Give the preparation type.
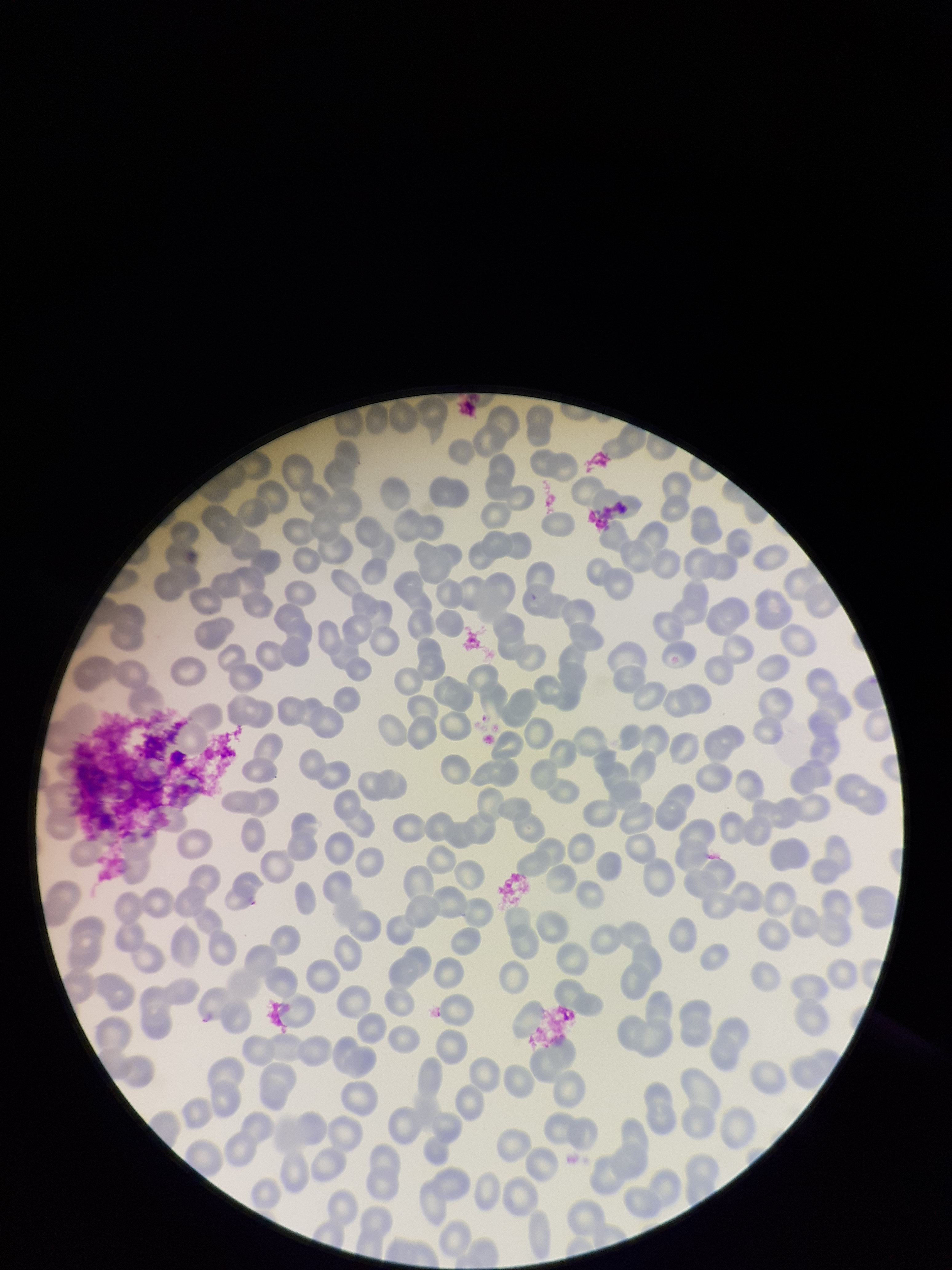
A thin smear.

Parasitized red blood cells: none detected. Image is 952×1270 pixels. Giemsa stain. Red blood cell count: 238. Patient malaria status: negative. Parasitized red blood cell count: 0. Single field of view. Photographed through the microscope eyepiece with a smartphone camera.